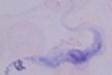
A trypanosome is shown. 1000x magnification. Micrograph.